Name the parasite shown.
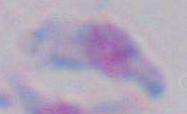
This is Toxoplasma gondii.

{
  "modality": "photomicrograph",
  "magnification": "1000x"
}